State which parasite is depicted.
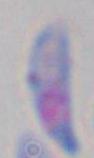
Toxoplasma gondii.

modality = micrograph
magnification = 1000x